Give the preparation type.
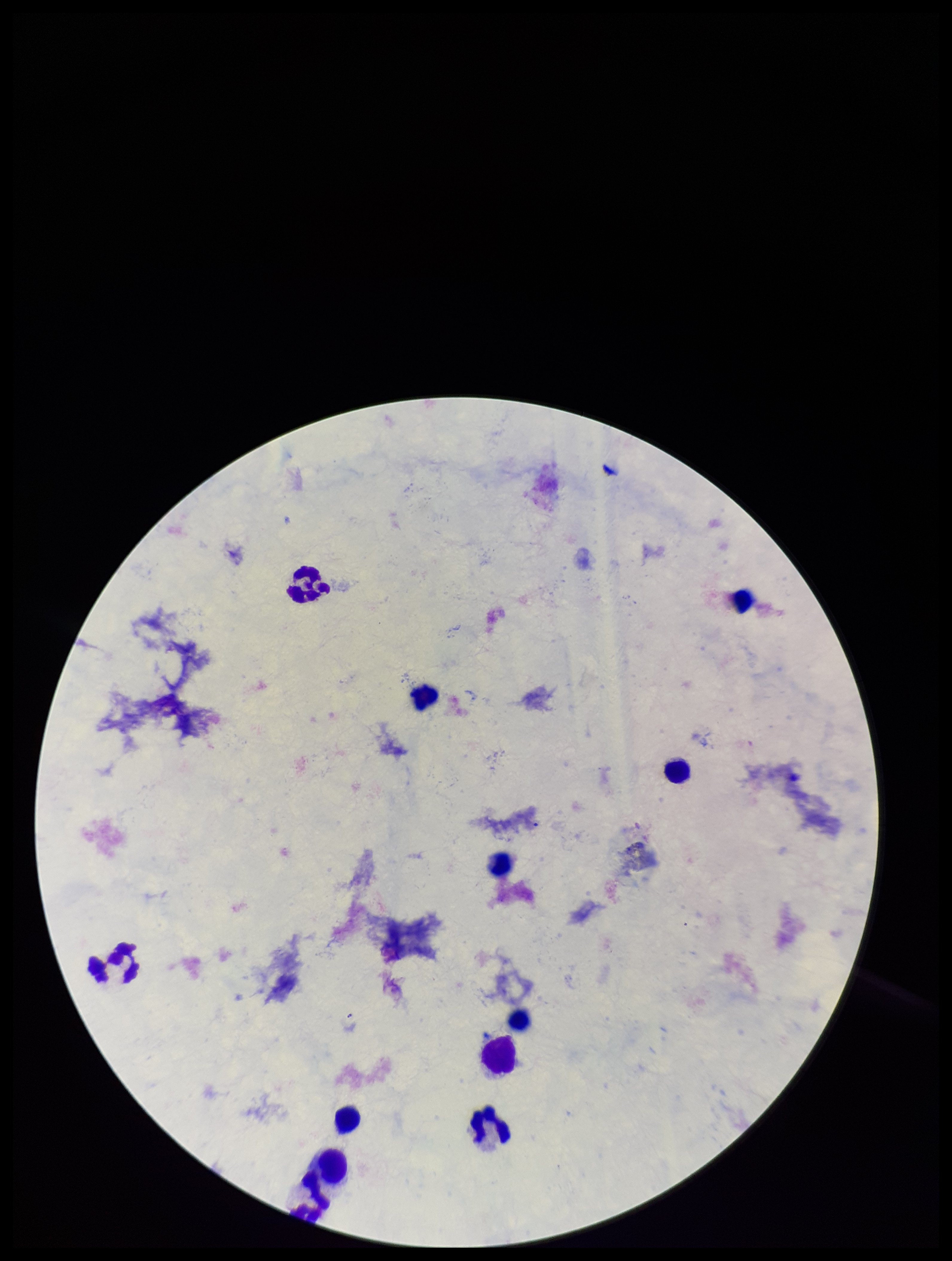
A thick smear.

plasmodium_parasites: none seen
image_size: 952×1261 pixels
stain: Giemsa
capture: smartphone photograph through the microscope eyepiece
patient_malaria_status: negative
field_of_view: single
parasite_count: 0
leukocyte_count: 12